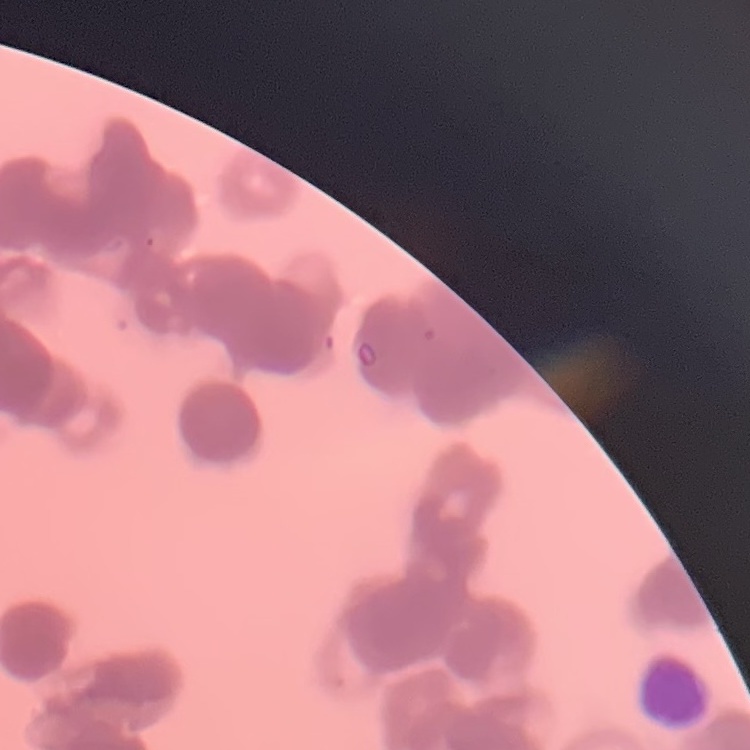 The red blood cells exhibit rouleaux formation. Field's or Giemsa stain. Square crop of a larger photomicrograph. Thin peripheral smear.